Assess the morphology of the red blood cells.
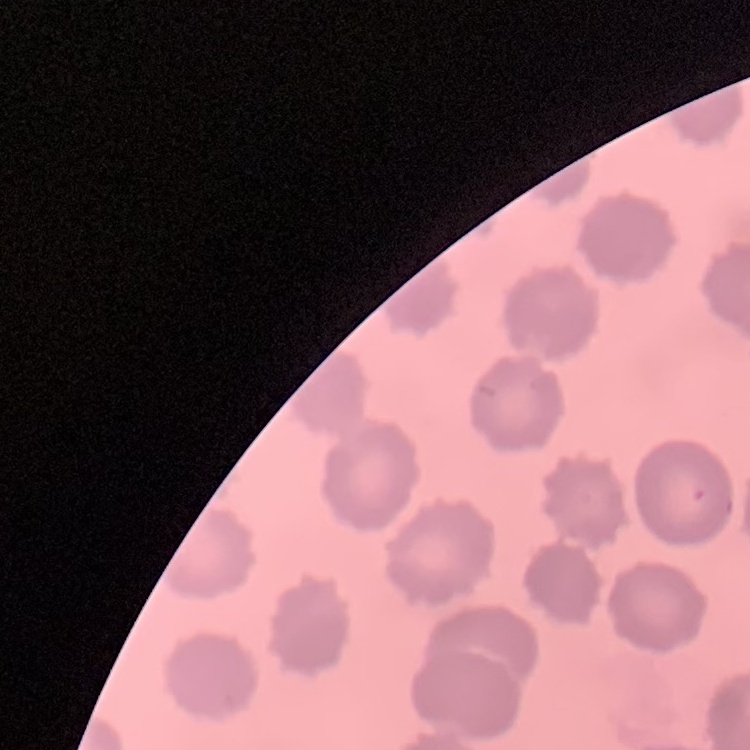
They show no rouleaux formation.

Summary:
  - Preparation: thin peripheral smear
  - Stain: Field's or Giemsa
  - Image type: square crop of a larger photomicrograph